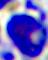
{
  "identification": "leukocyte",
  "magnification": "400x",
  "modality": "photomicrograph"
}